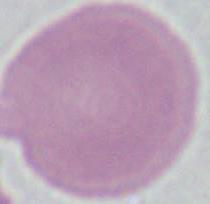

Photomicrograph. A red blood cell is shown. 1000x magnification.